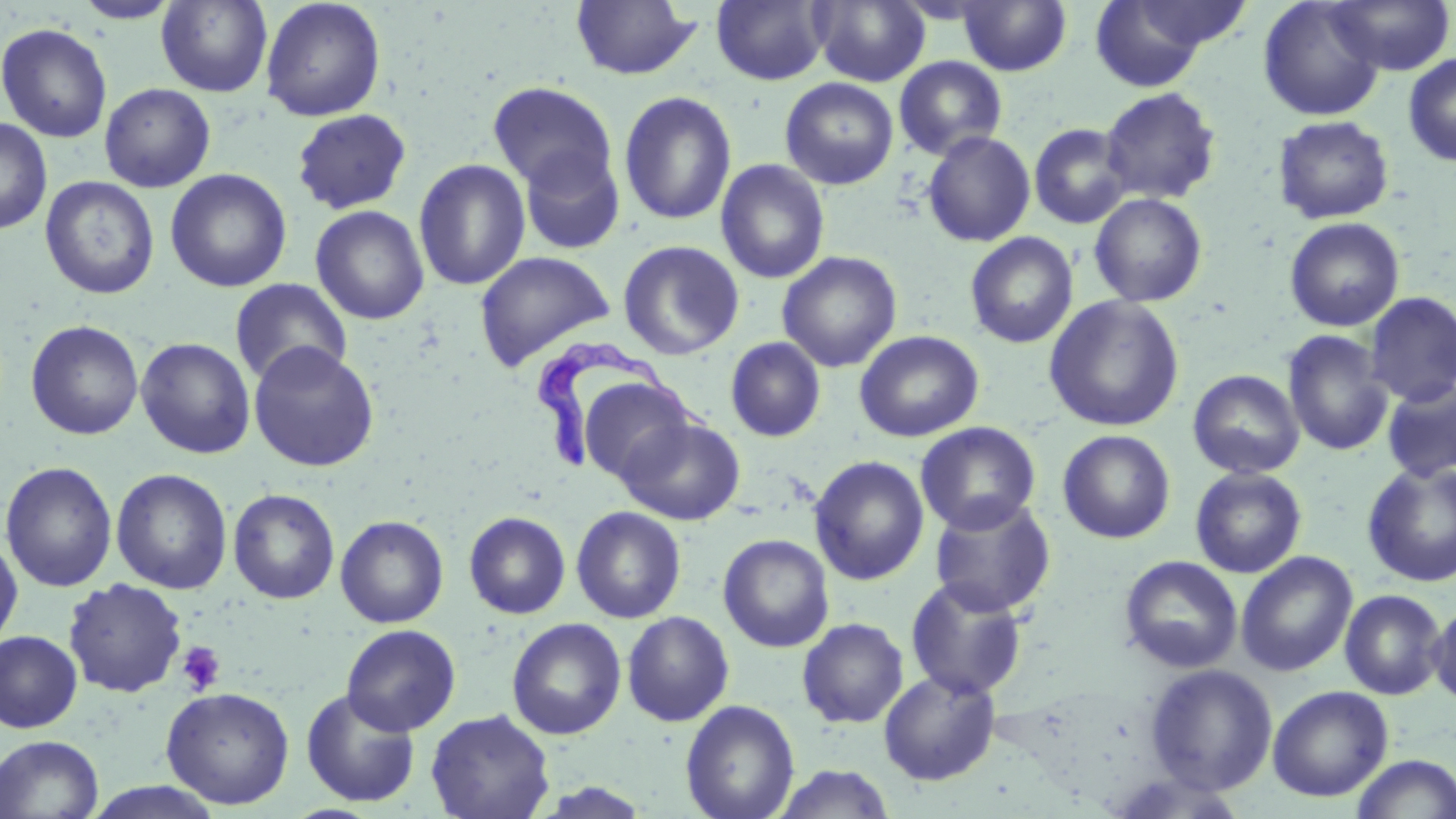 Approximate bounding boxes as (x1,y1)-(x2,y2) corner pairs in pixels. Platelet locations: (177,641)-(225,695). Uninfected red blood cell locations: (156,0)-(273,97), (711,0)-(829,85), (809,0)-(931,86), (957,0)-(1072,76), (1089,0)-(1225,92), (1257,0)-(1387,122), (1326,0)-(1455,75), (71,1)-(182,24), (260,1)-(386,121), (571,1)-(701,80), (1,23)-(112,143), (1403,52)-(1456,167), (893,56)-(1007,161), (780,77)-(899,190), (487,81)-(619,196), (99,82)-(216,193), (492,86)-(737,208), (1100,87)-(1221,204), (618,90)-(737,226), (290,108)-(413,215), (1274,115)-(1394,223), (0,116)-(52,236), (1028,123)-(1133,229), (922,130)-(1036,247), (516,145)-(626,255), (414,158)-(531,291), (715,159)-(830,284), (165,168)-(292,293), (40,176)-(160,299), (1089,193)-(1208,307), (310,205)-(430,325), (1284,217)-(1404,332), (965,232)-(1079,348), (618,240)-(744,360), (776,250)-(902,372), (474,251)-(615,371), (229,278)-(353,387), (1364,292)-(1456,406), (1044,295)-(1185,432), (26,319)-(144,440), (1282,329)-(1394,456), (854,330)-(984,442), (135,337)-(256,459), (725,337)-(826,442), (247,342)-(380,472), (1188,369)-(1304,479), (574,374)-(697,485), (1382,379)-(1456,482), (617,416)-(746,526), (915,421)-(1041,535), (1057,429)-(1176,544), (809,455)-(930,586), (1,460)-(118,593), (1361,461)-(1456,587), (1190,467)-(1307,578), (111,468)-(233,594), (228,488)-(340,604), (929,496)-(1056,617), (571,506)-(687,623), (464,511)-(571,619), (335,515)-(449,628), (0,534)-(23,653), (718,534)-(834,652), (1235,551)-(1358,677), (1118,555)-(1243,673), (905,577)-(1029,701), (63,578)-(188,697), (1339,589)-(1448,700), (1428,599)-(1456,708), (621,610)-(734,727), (506,617)-(627,740), (797,617)-(909,728), (341,623)-(461,736), (0,630)-(83,734), (1144,663)-(1279,794), (878,669)-(1001,786), (1267,685)-(1393,802), (161,686)-(295,809), (300,688)-(421,808), (680,699)-(800,819), (425,709)-(555,819), (0,735)-(104,818), (1350,753)-(1456,818), (769,764)-(897,819). Trypanosoma brucei locations: (532,338)-(717,473). Slide-level diagnosis: Trypanosoma brucei. Single field of view. Thin blood film. Captured at 1000x magnification. May-Grünwald-Giemsa-stained preparation. Light microscopy. Image is 1456×819 pixels.